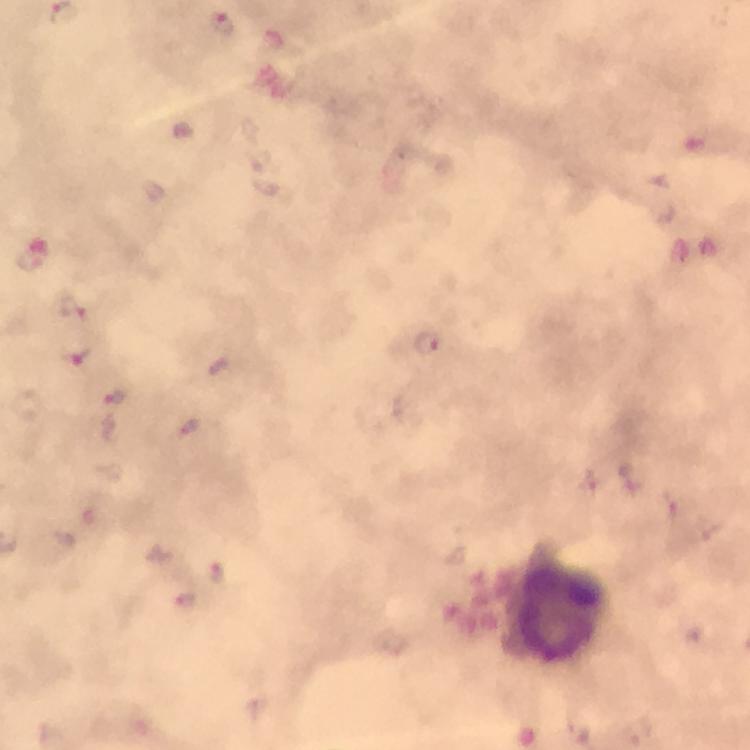
context = from a diagnostic examination for malaria
immersion oil = applied
magnification = 100x
image size = 750×750 pixels
leukocyte locations = approximate centers as {x, y} in pixels: {556, 611}
stain = Giemsa
cropped from = one field of view
capture = smartphone photograph through a microscope
Plasmodium parasite locations = approximate centers as {x, y} in pixels: {222, 24}, {153, 190}, {30, 258}, {73, 306}, {428, 343}, {75, 356}, {219, 364}, {116, 398}, {588, 478}, {707, 527}, {217, 573}, {184, 599}, {575, 731}, {637, 731}
preparation = thick smear